Locate every Plasmodium vivax-infected red blood cell.
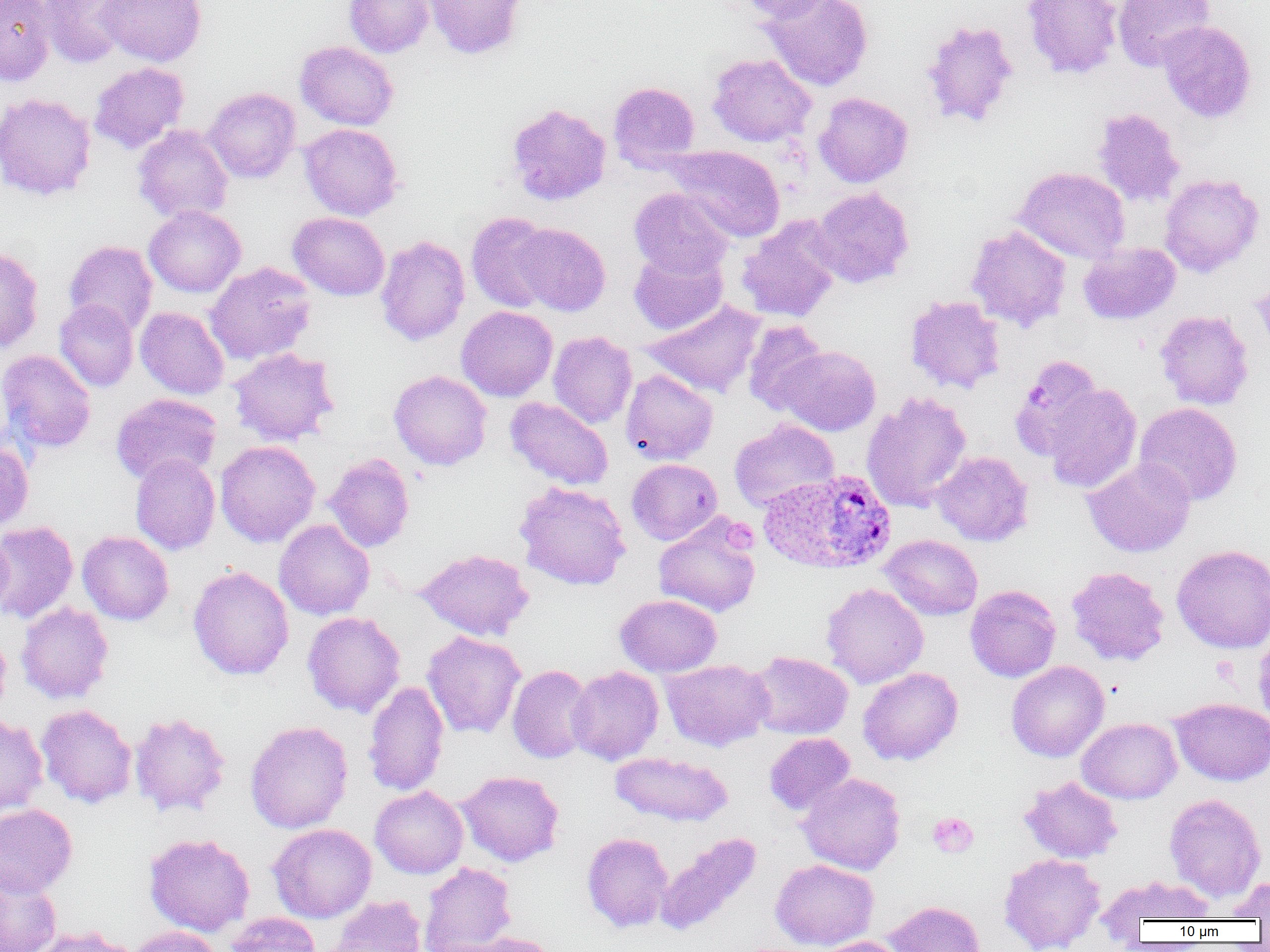
Approximate bounding boxes as (x1, y1, x2, y2) in pixels.
Plasmodium vivax-infected red blood cells: (759, 469, 897, 574).

slide-level diagnosis = Plasmodium vivax
image size = 1270×952 pixels
field of view = single
magnification = 1000x
modality = optical microscopy
preparation = thin blood smear
uninfected red blood cell locations = approximate bounding boxes as (x1, y1, x2, y2) in pixels: (0, 0, 55, 85), (37, 0, 135, 68), (97, 0, 206, 66), (344, 0, 434, 57), (424, 0, 525, 60), (734, 0, 836, 23), (762, 0, 873, 91), (1022, 0, 1123, 79), (1113, 0, 1215, 71), (920, 19, 1020, 128), (1157, 21, 1256, 123), (295, 41, 398, 130), (707, 54, 816, 147), (89, 62, 189, 154), (608, 81, 700, 171), (204, 87, 301, 183), (0, 92, 97, 201), (814, 92, 913, 188), (506, 102, 611, 206), (1091, 107, 1186, 208), (299, 123, 402, 221), (133, 124, 234, 223), (666, 145, 786, 242), (1013, 166, 1130, 263), (1159, 173, 1263, 277), (629, 187, 734, 278), (810, 188, 914, 288), (144, 205, 246, 297), (288, 212, 390, 301), (466, 212, 556, 313), (737, 218, 840, 323), (512, 223, 611, 316), (966, 225, 1072, 331), (375, 236, 470, 346), (64, 240, 158, 337), (1078, 242, 1180, 325), (0, 245, 44, 354), (629, 248, 728, 335), (204, 262, 316, 365), (1252, 271, 1270, 358), (905, 295, 1006, 394), (54, 299, 138, 392), (641, 300, 766, 399), (456, 306, 558, 401), (135, 307, 229, 399), (1155, 310, 1254, 410), (742, 320, 829, 415), (548, 331, 636, 429), (777, 345, 881, 436), (228, 347, 339, 446), (0, 349, 96, 453), (1009, 354, 1102, 459), (389, 369, 492, 470), (621, 369, 718, 465), (1043, 382, 1142, 493), (861, 391, 972, 513), (111, 392, 222, 485), (505, 397, 613, 490), (1133, 402, 1243, 506), (728, 419, 839, 511), (215, 440, 320, 547), (0, 441, 34, 533), (931, 451, 1033, 546), (324, 453, 415, 552), (130, 454, 220, 555), (626, 458, 723, 545), (1082, 458, 1196, 558), (514, 481, 631, 590), (653, 514, 761, 617), (274, 519, 375, 620), (0, 521, 78, 624), (0, 530, 12, 621), (77, 531, 174, 625), (880, 534, 982, 620), (1171, 544, 1270, 654), (414, 548, 534, 641), (188, 565, 294, 680), (1066, 566, 1170, 666), (821, 582, 928, 689), (965, 585, 1061, 682), (615, 594, 722, 677), (16, 602, 114, 704), (302, 611, 405, 718), (1253, 627, 1270, 730), (0, 630, 11, 720), (422, 631, 525, 739), (748, 651, 853, 739), (660, 659, 774, 751), (1006, 660, 1109, 762), (507, 664, 595, 763), (567, 666, 664, 765), (858, 667, 964, 766), (362, 681, 449, 797), (1170, 697, 1270, 786), (36, 704, 137, 808), (129, 711, 231, 818), (0, 714, 47, 818), (1077, 717, 1181, 804), (245, 720, 353, 833), (764, 732, 855, 815), (610, 751, 733, 827), (456, 770, 565, 866), (797, 773, 905, 875), (1019, 775, 1123, 863), (370, 786, 468, 879), (1164, 793, 1267, 902), (0, 804, 77, 897), (268, 823, 376, 923), (654, 832, 762, 935), (144, 833, 255, 936), (582, 833, 673, 932), (998, 853, 1105, 952), (770, 859, 879, 950), (419, 862, 517, 952), (0, 872, 62, 952), (1095, 875, 1215, 933), (1228, 875, 1270, 922), (326, 895, 426, 952), (885, 900, 985, 952), (225, 913, 321, 952), (27, 926, 137, 952), (128, 926, 221, 952), (442, 931, 563, 952), (814, 936, 908, 952)
platelet locations = approximate bounding boxes as (x1, y1, x2, y2) in pixels: (723, 518, 758, 555), (927, 812, 978, 858)